State which parasite is depicted.
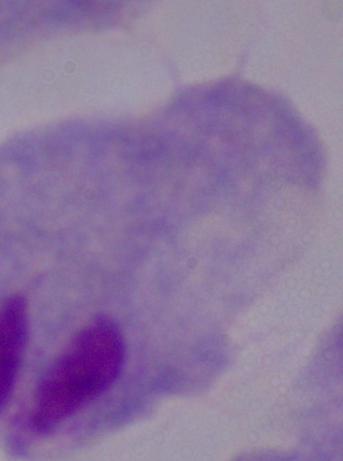

This is a trichomonad.

Photomicrograph. 1000x magnification.